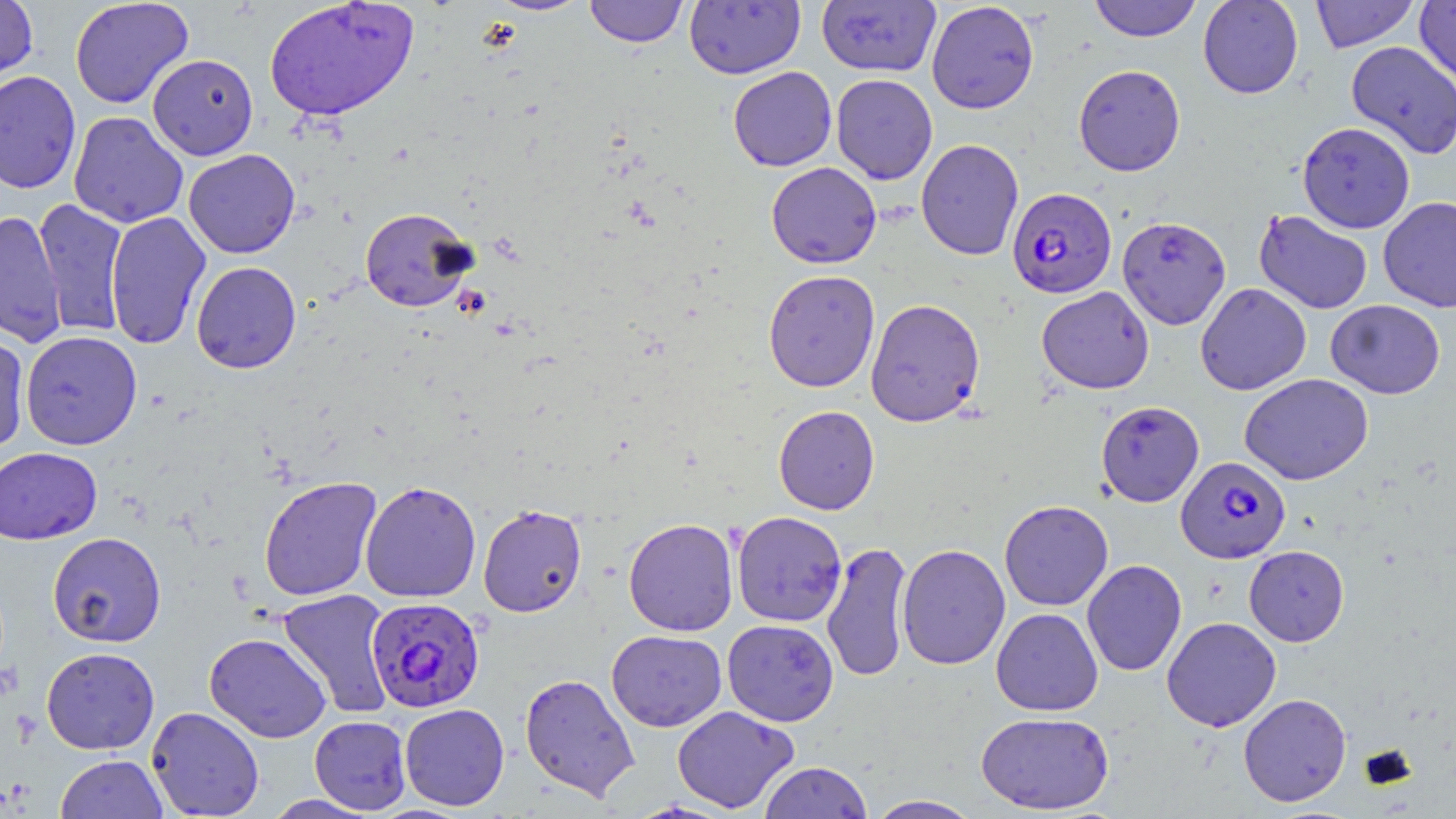

Approximate bounding boxes as (x1, y1, x2, y2) in pixels. Uninfected red blood cell locations: (69, 0, 194, 109), (264, 0, 419, 122), (486, 0, 592, 16), (584, 0, 688, 47), (1089, 0, 1202, 42), (1198, 0, 1303, 99), (1310, 0, 1419, 52), (1415, 0, 1456, 91), (0, 1, 38, 86), (684, 1, 805, 79), (816, 1, 941, 77), (926, 1, 1039, 114), (1345, 41, 1456, 159), (148, 54, 259, 160), (1073, 64, 1186, 176), (728, 66, 837, 171), (0, 70, 82, 194), (831, 74, 938, 184), (68, 111, 189, 229), (1297, 121, 1415, 233), (916, 138, 1024, 260), (183, 149, 300, 258), (766, 162, 882, 269), (1378, 196, 1456, 312), (34, 199, 129, 337), (359, 207, 478, 312), (1254, 209, 1373, 314), (0, 210, 68, 349), (105, 211, 212, 349), (1117, 216, 1232, 329), (191, 261, 302, 374), (763, 269, 881, 392), (1195, 283, 1311, 396), (1036, 286, 1154, 394), (865, 298, 985, 427), (1326, 299, 1446, 399), (0, 330, 31, 454), (20, 331, 142, 450), (1239, 373, 1374, 485), (1096, 400, 1204, 506), (773, 405, 880, 515), (0, 447, 102, 545), (258, 476, 382, 601), (360, 480, 482, 602), (999, 499, 1114, 611), (477, 503, 587, 618), (732, 511, 847, 627), (623, 517, 739, 636), (47, 532, 166, 647), (821, 541, 913, 684), (897, 543, 1011, 670), (1244, 545, 1349, 646), (1081, 559, 1187, 676), (277, 588, 396, 719), (991, 608, 1103, 716), (1161, 616, 1282, 731), (722, 619, 839, 726), (606, 630, 727, 732), (204, 632, 332, 742), (41, 647, 160, 754), (519, 673, 640, 801), (1238, 693, 1351, 807), (399, 703, 509, 811), (672, 705, 799, 813), (146, 706, 264, 818), (976, 711, 1114, 814), (309, 715, 411, 814), (55, 754, 169, 818), (758, 761, 872, 819), (262, 794, 377, 818), (865, 795, 983, 818). Plasmodium falciparum-infected red blood cell locations: (1007, 187, 1116, 298), (1176, 456, 1290, 563), (365, 596, 486, 713). Slide-level diagnosis: Plasmodium falciparum. Optical microscopy. Image is 1456×819 pixels. Captured at 1000x magnification. May-Grünwald-Giemsa-stained preparation. Thin blood smear. One field of a larger specimen.